Locate and identify every blood parasite.
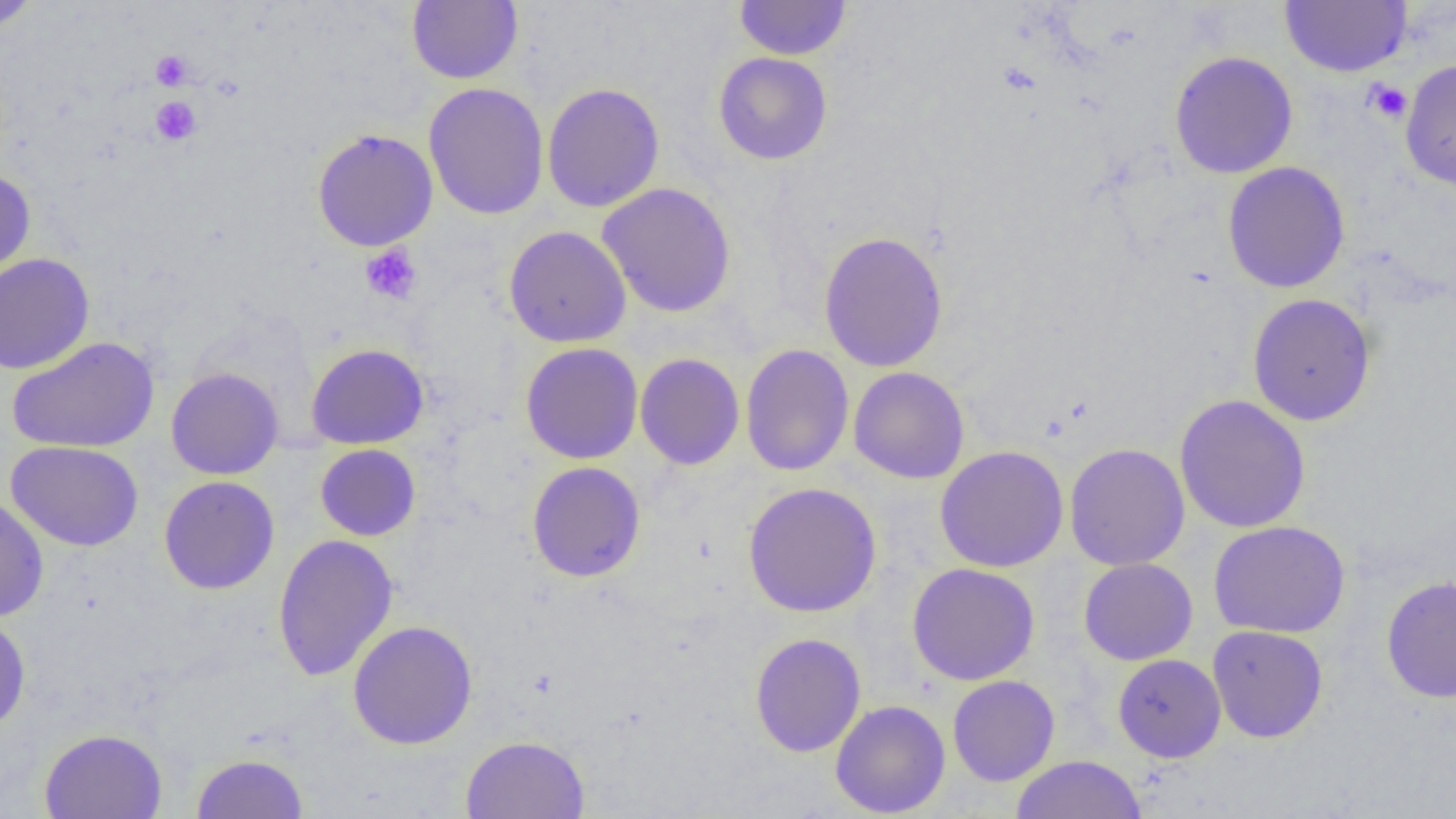

No blood parasites seen.

slide-level diagnosis = no evidence of blood parasites
field of view = one of a larger specimen
platelet locations = approximate bounding boxes as (x1, y1, x2, y2) in pixels: (151, 50, 192, 90), (1363, 79, 1413, 124), (151, 96, 201, 146), (359, 243, 422, 305)
modality = optical microscopy
image size = 1456×819 pixels
preparation = thin blood film
uninfected red blood cell locations = approximate bounding boxes as (x1, y1, x2, y2) in pixels: (0, 0, 40, 33), (407, 0, 523, 84), (734, 0, 852, 60), (1279, 0, 1412, 77), (1169, 51, 1298, 179), (713, 52, 832, 165), (1400, 58, 1456, 193), (423, 82, 550, 220), (541, 82, 665, 212), (312, 128, 438, 251), (1222, 161, 1350, 294), (0, 168, 36, 281), (597, 182, 737, 318), (504, 225, 632, 347), (818, 230, 949, 372), (0, 253, 95, 374), (1247, 293, 1376, 426), (7, 337, 159, 454), (520, 342, 643, 464), (306, 343, 429, 449), (740, 344, 855, 477), (635, 353, 745, 470), (166, 367, 284, 480), (848, 367, 970, 484), (1174, 394, 1311, 534), (5, 440, 144, 552), (1064, 442, 1190, 571), (315, 444, 421, 541), (935, 445, 1069, 573), (526, 461, 646, 582), (159, 475, 280, 595), (742, 481, 882, 618), (0, 496, 49, 622), (1209, 520, 1350, 638), (272, 534, 399, 681), (1078, 557, 1198, 665), (907, 563, 1040, 685), (1380, 575, 1456, 704), (0, 613, 31, 733), (348, 620, 478, 749), (1207, 625, 1328, 743), (750, 632, 866, 757), (1112, 653, 1226, 762), (947, 675, 1060, 786), (830, 699, 951, 818), (39, 728, 168, 819), (460, 735, 590, 818), (191, 752, 308, 818), (1010, 754, 1147, 818)
magnification = 1000x